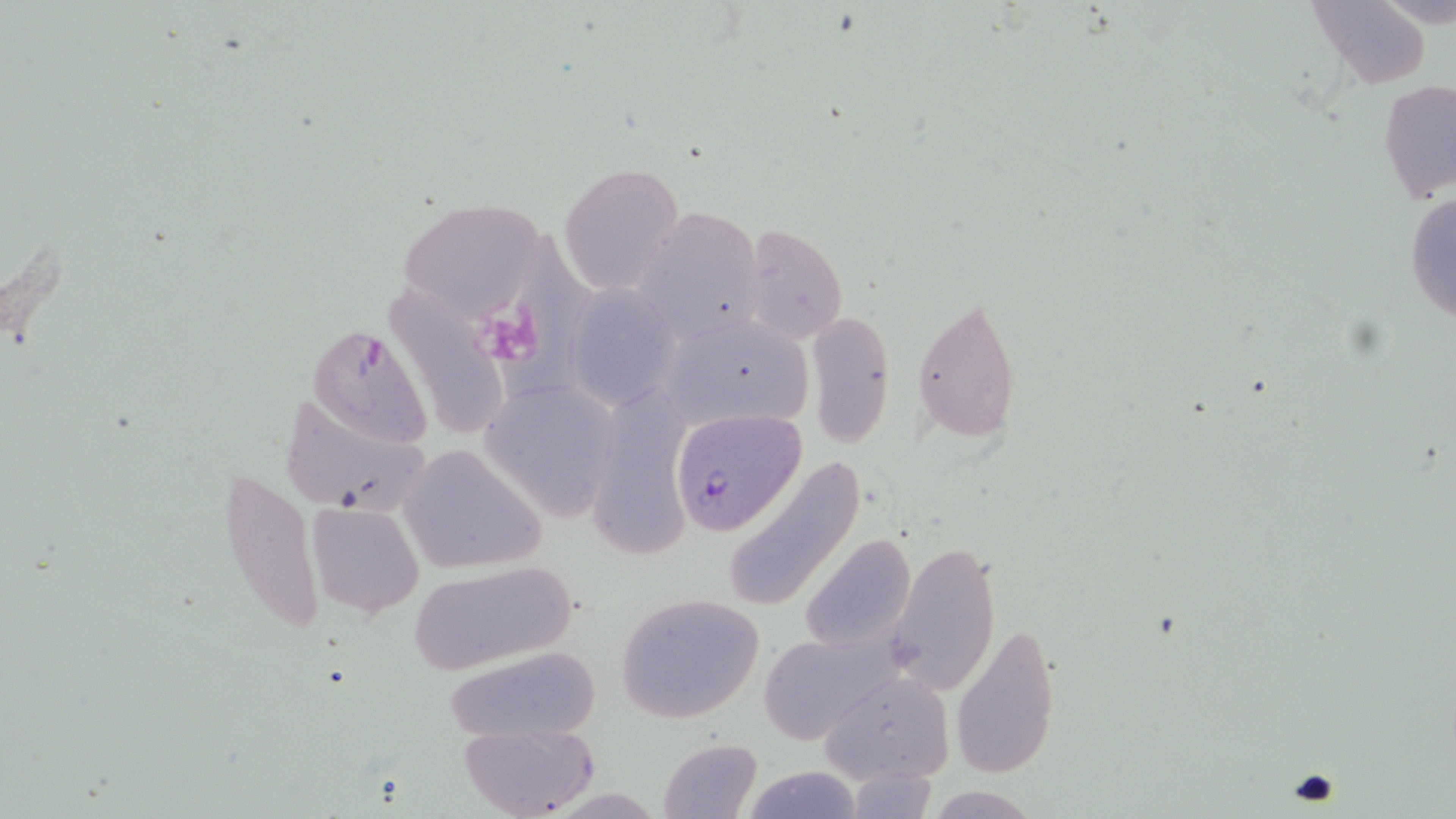 Approximate bounding boxes as (x1, y1, x2, y2) in pixels. Uninfected red blood cell locations: (1306, 0, 1434, 90), (1377, 80, 1455, 204), (557, 161, 685, 295), (1404, 188, 1456, 326), (396, 198, 551, 325), (633, 206, 767, 342), (485, 222, 601, 412), (738, 224, 848, 346), (562, 285, 683, 412), (370, 288, 508, 453), (912, 293, 1022, 440), (806, 313, 895, 448), (661, 315, 818, 436), (305, 323, 436, 449), (483, 382, 621, 523), (589, 391, 693, 558), (279, 393, 430, 515), (398, 443, 548, 575), (721, 455, 868, 617), (216, 460, 325, 640), (305, 501, 425, 618), (800, 534, 917, 651), (885, 542, 999, 698), (407, 560, 578, 675), (614, 592, 766, 723), (953, 624, 1061, 779), (758, 631, 896, 743), (440, 646, 602, 741), (819, 669, 953, 786), (459, 723, 597, 819), (658, 737, 762, 818), (846, 765, 940, 818), (741, 766, 867, 819). Plasmodium falciparum-infected red blood cell locations: (670, 408, 804, 534). Platelet locations: (487, 308, 546, 367). Slide-level diagnosis: Plasmodium falciparum. Optical microscopy. Image is 1456×819 pixels. One field of a larger specimen. May-Grünwald-Giemsa stain. Thin blood film. 1000x magnification.